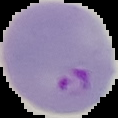
Result: Plasmodium parasites detected. From a thin blood film. Image is 118×118 pixels. Cell region segmented out of the field of view; the surrounding area is masked to black.